Name the parasite shown.
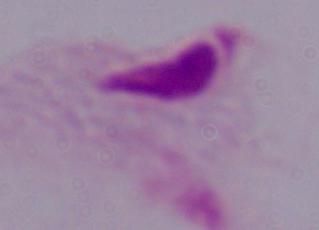
A trichomonad.

modality: micrograph
magnification: 1000x